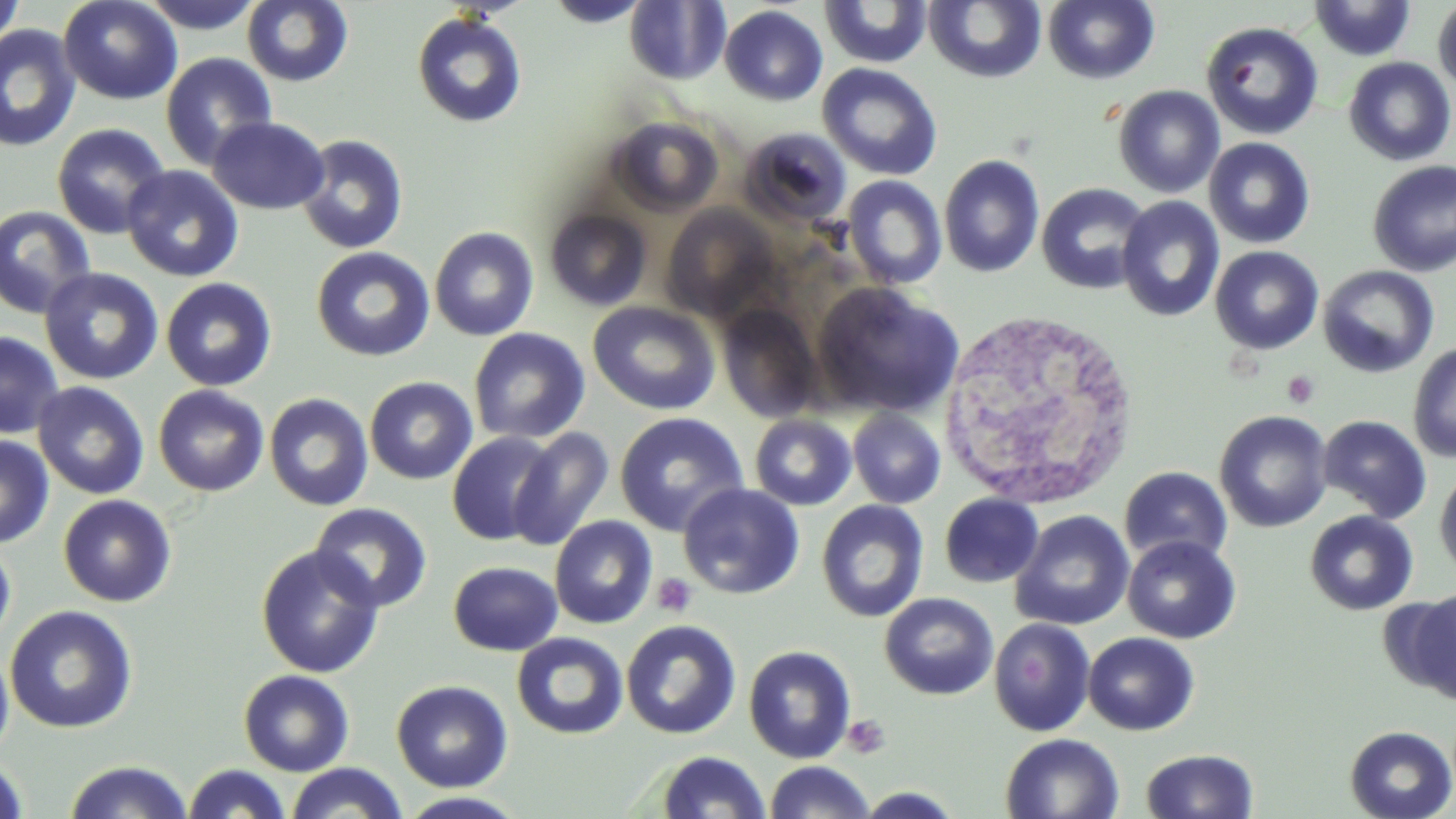

Approximate bounding boxes as (x1, y1, x2, y2) in pixels. White blood cell locations: (935, 307, 1140, 510). Uninfected red blood cell locations: (0, 0, 23, 55), (58, 0, 183, 105), (138, 0, 266, 33), (241, 0, 353, 87), (544, 0, 652, 27), (923, 0, 1048, 84), (1309, 0, 1417, 61), (623, 1, 730, 84), (819, 1, 933, 68), (1042, 1, 1160, 85), (1433, 1, 1456, 94), (719, 5, 828, 106), (411, 12, 527, 127), (1201, 22, 1324, 140), (0, 24, 81, 152), (160, 52, 277, 170), (1342, 57, 1455, 166), (817, 63, 943, 180), (1112, 84, 1225, 198), (207, 116, 330, 214), (607, 116, 723, 218), (51, 123, 171, 240), (738, 127, 852, 229), (295, 134, 409, 254), (1203, 137, 1315, 249), (938, 154, 1045, 278), (1367, 160, 1456, 277), (122, 165, 244, 282), (842, 175, 947, 290), (1035, 182, 1152, 295), (1116, 196, 1225, 323), (0, 205, 97, 319), (661, 205, 778, 320), (544, 207, 652, 311), (429, 226, 539, 341), (310, 246, 436, 361), (1210, 246, 1324, 354), (1318, 265, 1439, 378), (39, 267, 163, 385), (160, 277, 277, 392), (812, 282, 964, 419), (587, 301, 721, 415), (715, 305, 822, 423), (468, 327, 590, 445), (0, 331, 66, 440), (1407, 341, 1456, 464), (364, 376, 477, 485), (32, 381, 149, 500), (153, 385, 270, 496), (264, 392, 374, 510), (848, 407, 946, 509), (1214, 410, 1333, 533), (614, 411, 749, 536), (749, 413, 857, 511), (1318, 415, 1432, 523), (508, 427, 614, 551), (447, 432, 558, 546), (0, 433, 54, 548), (1119, 466, 1233, 568), (1434, 467, 1456, 579), (678, 483, 806, 600), (939, 493, 1043, 588), (57, 494, 177, 607), (816, 500, 929, 623), (309, 502, 433, 613), (1011, 510, 1135, 631), (1304, 511, 1418, 616), (549, 515, 658, 629), (1122, 535, 1241, 644), (0, 537, 16, 653), (255, 544, 384, 678), (448, 561, 562, 656), (1394, 590, 1456, 702), (879, 593, 998, 700), (4, 605, 138, 733), (989, 618, 1095, 737), (621, 620, 741, 739), (1083, 632, 1199, 735), (511, 633, 628, 740), (0, 644, 14, 762), (743, 645, 856, 763), (238, 669, 354, 776), (392, 679, 512, 792), (1344, 725, 1456, 818), (999, 733, 1125, 818), (1141, 749, 1259, 818), (656, 750, 770, 819), (0, 756, 31, 819), (63, 759, 194, 818), (763, 761, 876, 818), (285, 762, 409, 819), (182, 763, 292, 818), (853, 787, 966, 818), (395, 791, 531, 818). Platelet locations: (1282, 370, 1320, 408), (652, 572, 697, 618), (842, 714, 891, 759). Slide-level diagnosis: no evidence of blood parasites. Captured at 1000x magnification. Thin blood film. Image is 1456×819 pixels. May-Grünwald-Giemsa stain. Single field of view. Light microscopy.